Assess the morphology of the red blood cells.
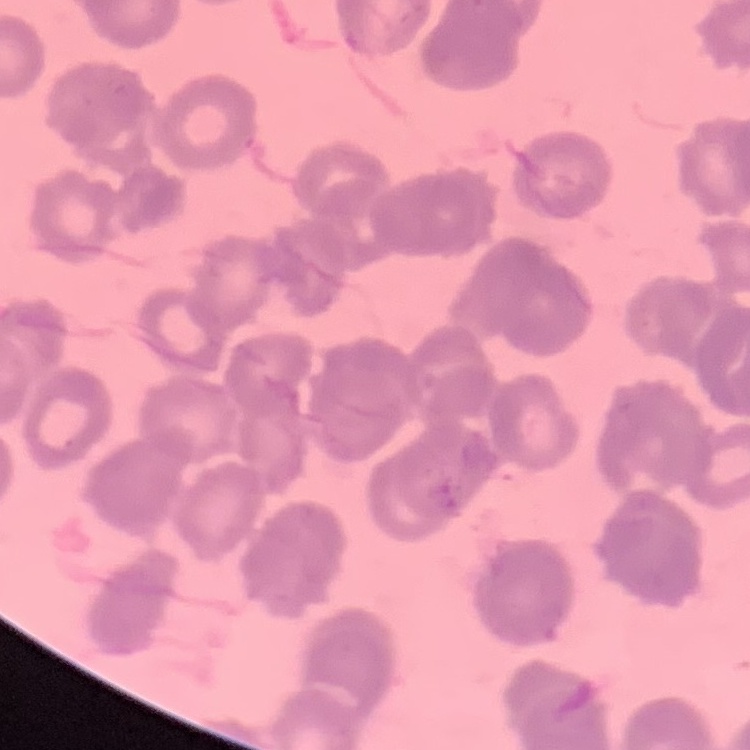
They show rouleaux formation.

Square crop of a larger photomicrograph. Field's or Giemsa stain. Thin blood film.